Report the malaria status of this cell.
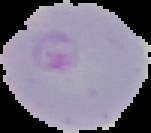

Parasitized.

From a thin blood smear. Image is 151×133 pixels. Cell region segmented out of the field of view; the surrounding area is masked to black.